Comment on the morphology of the red blood cells.
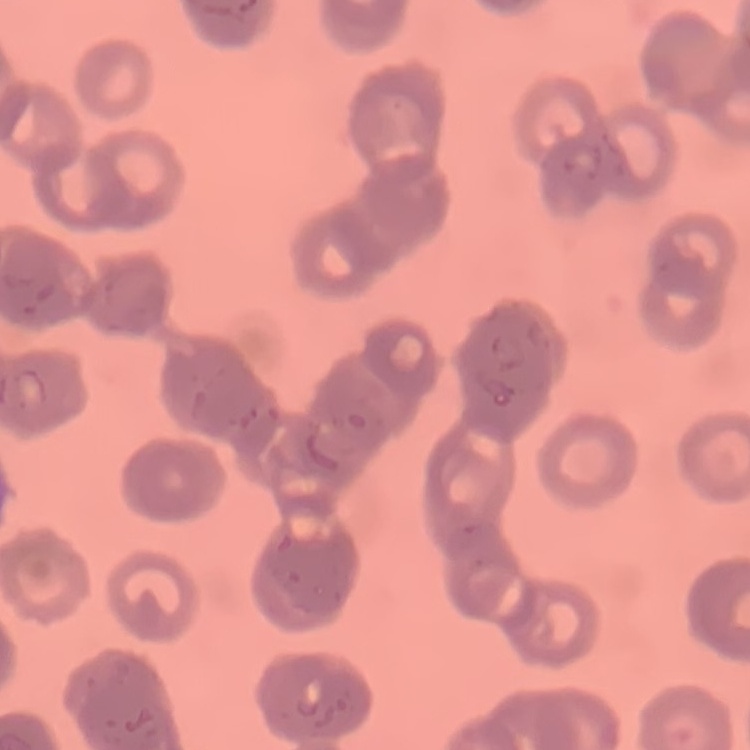
They show rouleaux formation.

Summary:
  - Preparation: thin blood smear
  - Image type: one tile cut from a larger photomicrograph
  - Stain: Field's or Giemsa